Describe the morphology of the red blood cells.
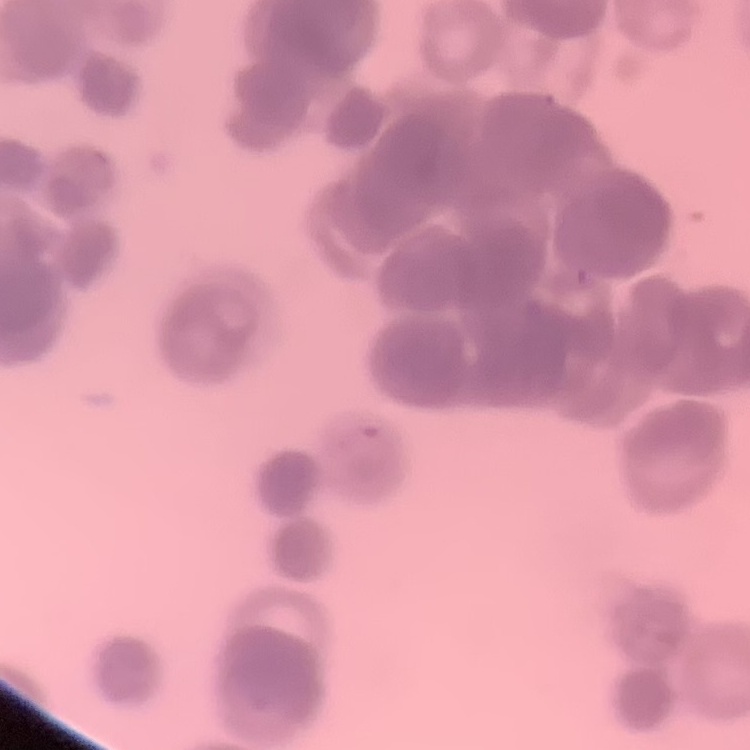

They show rouleaux formation.

Stained with either Field's or Giemsa. One tile cut from a larger photomicrograph. Thin blood film.